Outline each blood parasite and name the species.
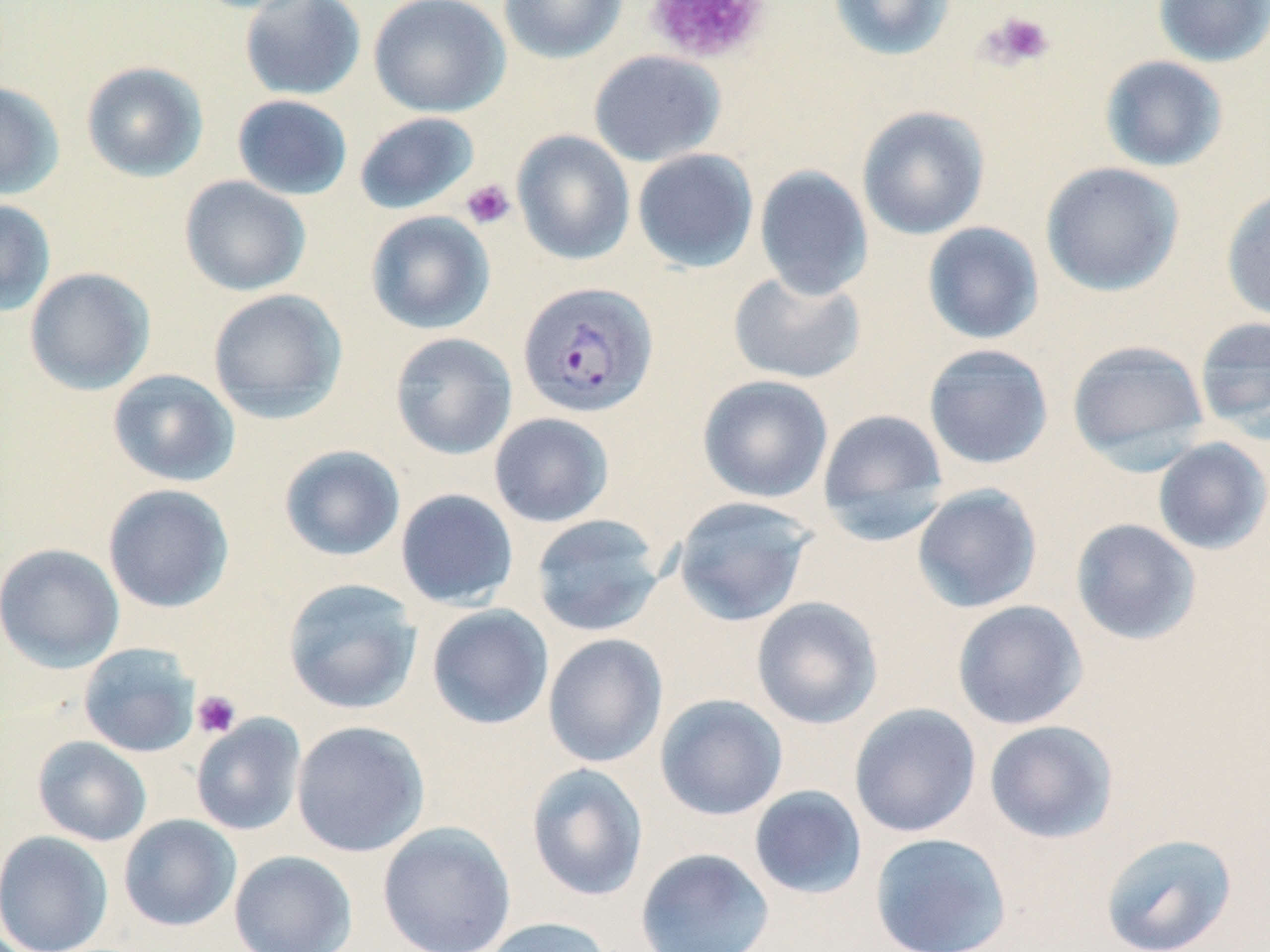
Approximate bounding boxes as named x1/y1/x2/y2 corners in pixels.
Plasmodium vivax-infected red blood cells: (x1=517, y1=281, x2=658, y2=418).
No Plasmodium falciparum, Plasmodium ovale, Plasmodium malariae, Babesia divergens, or Trypanosoma brucei observed.

slide-level diagnosis = Plasmodium vivax
stain = May-Grünwald-Giemsa
magnification = 1000x
modality = optical microscopy
field of view = one of a larger specimen
platelet locations = approximate bounding boxes as named x1/y1/x2/y2 corners in pixels: (x1=645, y1=0, x2=771, y2=65), (x1=980, y1=11, x2=1056, y2=70), (x1=460, y1=179, x2=515, y2=230), (x1=191, y1=690, x2=242, y2=739)
preparation = thin blood film
uninfected red blood cell locations = approximate bounding boxes as named x1/y1/x2/y2 corners in pixels: (x1=238, y1=0, x2=367, y2=101), (x1=368, y1=0, x2=510, y2=118), (x1=499, y1=0, x2=628, y2=63), (x1=828, y1=0, x2=957, y2=62), (x1=1152, y1=0, x2=1270, y2=67), (x1=588, y1=50, x2=726, y2=166), (x1=1099, y1=55, x2=1229, y2=173), (x1=80, y1=61, x2=208, y2=182), (x1=0, y1=81, x2=65, y2=200), (x1=231, y1=94, x2=353, y2=201), (x1=857, y1=106, x2=990, y2=240), (x1=354, y1=111, x2=480, y2=215), (x1=511, y1=130, x2=635, y2=265), (x1=631, y1=148, x2=759, y2=273), (x1=1040, y1=161, x2=1185, y2=297), (x1=754, y1=166, x2=873, y2=300), (x1=179, y1=175, x2=312, y2=297), (x1=1221, y1=187, x2=1270, y2=322), (x1=0, y1=198, x2=56, y2=317), (x1=365, y1=210, x2=496, y2=335), (x1=921, y1=222, x2=1044, y2=345), (x1=24, y1=267, x2=156, y2=395), (x1=728, y1=270, x2=867, y2=384), (x1=207, y1=288, x2=348, y2=423), (x1=1193, y1=316, x2=1270, y2=441), (x1=390, y1=332, x2=517, y2=460), (x1=1066, y1=339, x2=1210, y2=467), (x1=922, y1=344, x2=1054, y2=470), (x1=107, y1=368, x2=240, y2=487), (x1=697, y1=375, x2=834, y2=503), (x1=817, y1=408, x2=950, y2=542), (x1=489, y1=412, x2=615, y2=528), (x1=1152, y1=437, x2=1270, y2=554), (x1=279, y1=445, x2=406, y2=562), (x1=103, y1=484, x2=235, y2=613), (x1=911, y1=484, x2=1043, y2=613), (x1=395, y1=488, x2=519, y2=610), (x1=672, y1=495, x2=815, y2=627), (x1=531, y1=514, x2=667, y2=637), (x1=1070, y1=518, x2=1202, y2=646), (x1=0, y1=543, x2=125, y2=672), (x1=283, y1=578, x2=422, y2=714), (x1=751, y1=596, x2=883, y2=729), (x1=951, y1=600, x2=1088, y2=730), (x1=426, y1=604, x2=554, y2=730), (x1=542, y1=633, x2=669, y2=768), (x1=78, y1=643, x2=201, y2=757), (x1=655, y1=694, x2=788, y2=821), (x1=849, y1=703, x2=982, y2=838), (x1=190, y1=714, x2=306, y2=835), (x1=291, y1=720, x2=430, y2=857), (x1=984, y1=720, x2=1119, y2=844), (x1=32, y1=736, x2=152, y2=846), (x1=526, y1=763, x2=649, y2=902), (x1=748, y1=785, x2=868, y2=901), (x1=118, y1=814, x2=241, y2=932), (x1=377, y1=820, x2=516, y2=952), (x1=0, y1=830, x2=113, y2=952), (x1=869, y1=832, x2=1012, y2=952), (x1=1100, y1=833, x2=1237, y2=952), (x1=635, y1=847, x2=775, y2=952), (x1=229, y1=850, x2=357, y2=952), (x1=480, y1=917, x2=613, y2=952)
image size = 1270×952 pixels